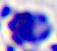

identification: leukocyte
magnification: 400x
modality: micrograph